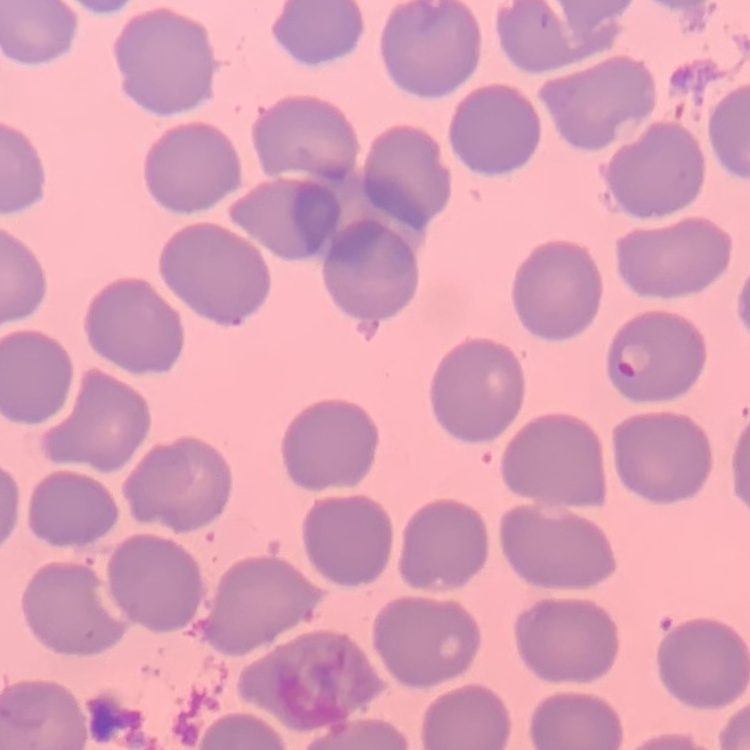

erythrocyte morphology = no rouleaux formation
preparation = thin blood film
stain = Field's or Giemsa
image type = one tile cut from a larger photomicrograph